Point out each leukocyte.
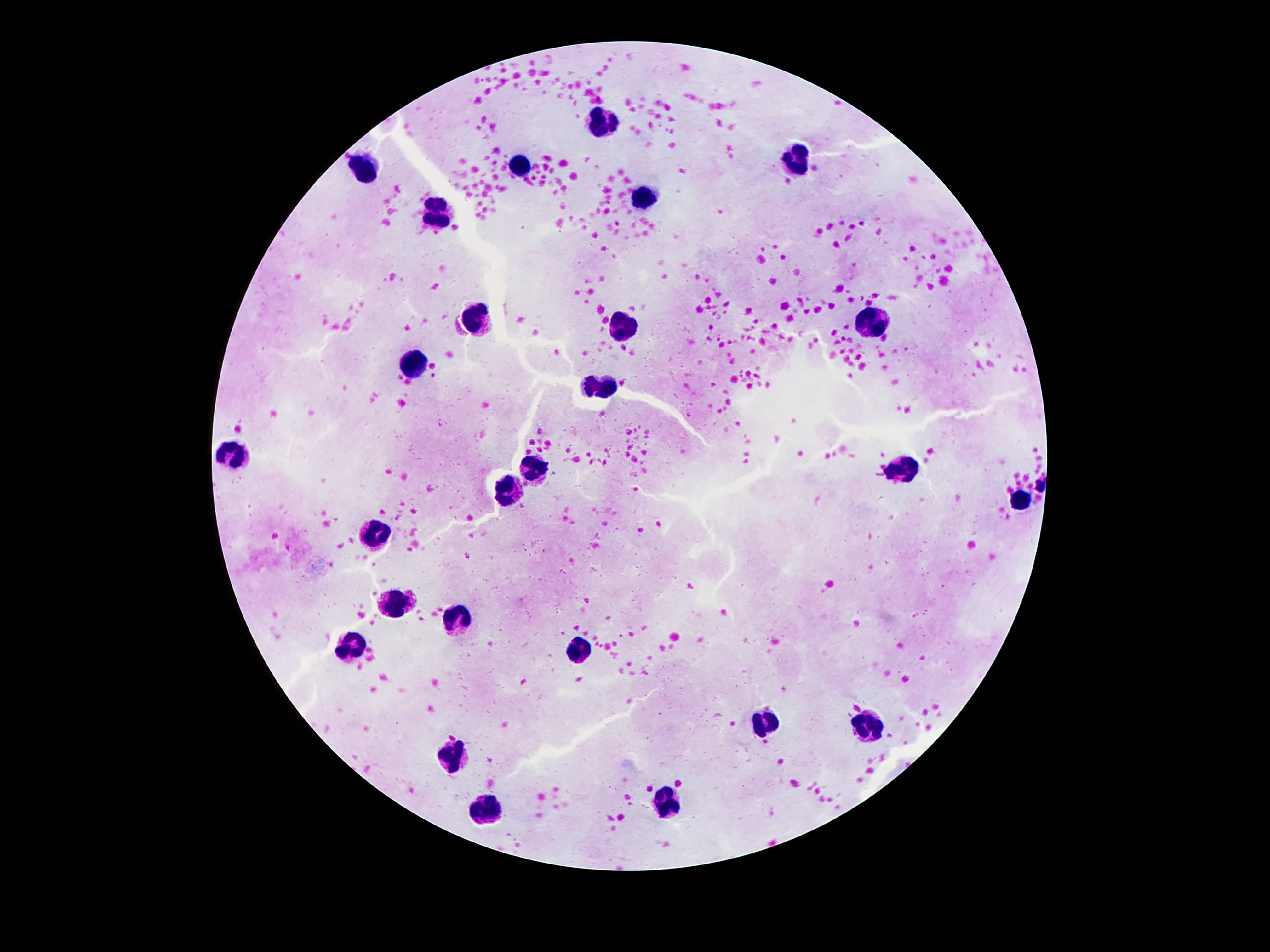
Approximate centers as [x, y] in pixels.
Leukocytes: [601, 123], [796, 160], [519, 164], [362, 169], [643, 200], [435, 214], [479, 320], [622, 324], [870, 326], [416, 363], [599, 384], [229, 454], [536, 467], [903, 468], [511, 491], [1017, 500], [381, 535], [395, 600], [456, 622], [355, 647], [578, 648], [765, 723], [868, 732], [454, 753], [666, 805], [483, 808].

capture = smartphone camera through the microscope eyepiece
patient malaria status = negative
magnification = 100x
preparation = thick blood film
stain = Giemsa
field of view = one from this slide
image size = 1270×952 pixels